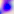
400x magnification. Toxoplasma gondii is seen. Micrograph.